Assess this cell for malaria.
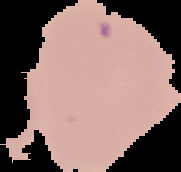
It is uninfected.

Summary:
  - Image type: segmented cell region on a black background
  - Preparation: thin blood film
  - Image size: 181×172 pixels